Assess this cell for malaria.
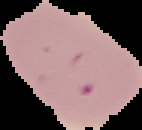
Uninfected.

Summary:
  - Image type: segmented cell region with the area outside set to black
  - Image size: 142×130 pixels
  - Preparation: thin blood smear